Report the malaria status of this cell.
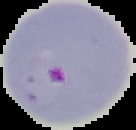
Parasitized.

Segmented cell region on a black background. Image is 136×130 pixels. From a thin blood smear.